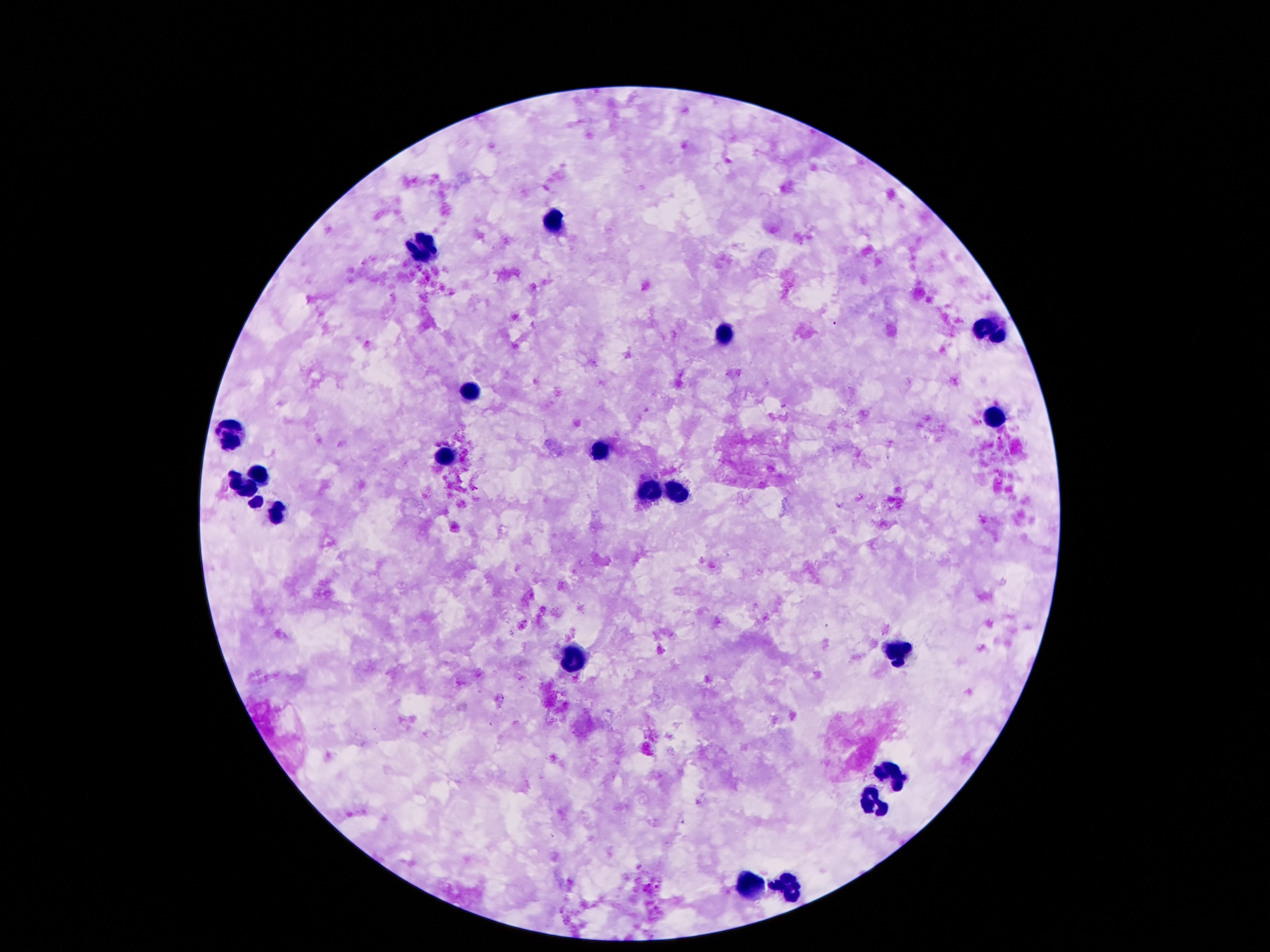
Approximate centers as [x, y] in pixels.
Summary:
  - Leukocyte locations: [554, 225], [423, 244], [992, 328], [724, 334], [474, 392], [994, 414], [234, 432], [447, 454], [599, 454], [259, 477], [240, 488], [678, 492], [650, 494], [253, 502], [281, 510], [896, 650], [576, 654], [892, 775], [875, 802], [789, 885], [754, 887]
  - Stain: Giemsa
  - Field of view: single
  - Capture: smartphone camera through the microscope eyepiece
  - Magnification: 100x
  - Image size: 1270×952 pixels
  - Patient malaria status: negative
  - Preparation: thick blood smear